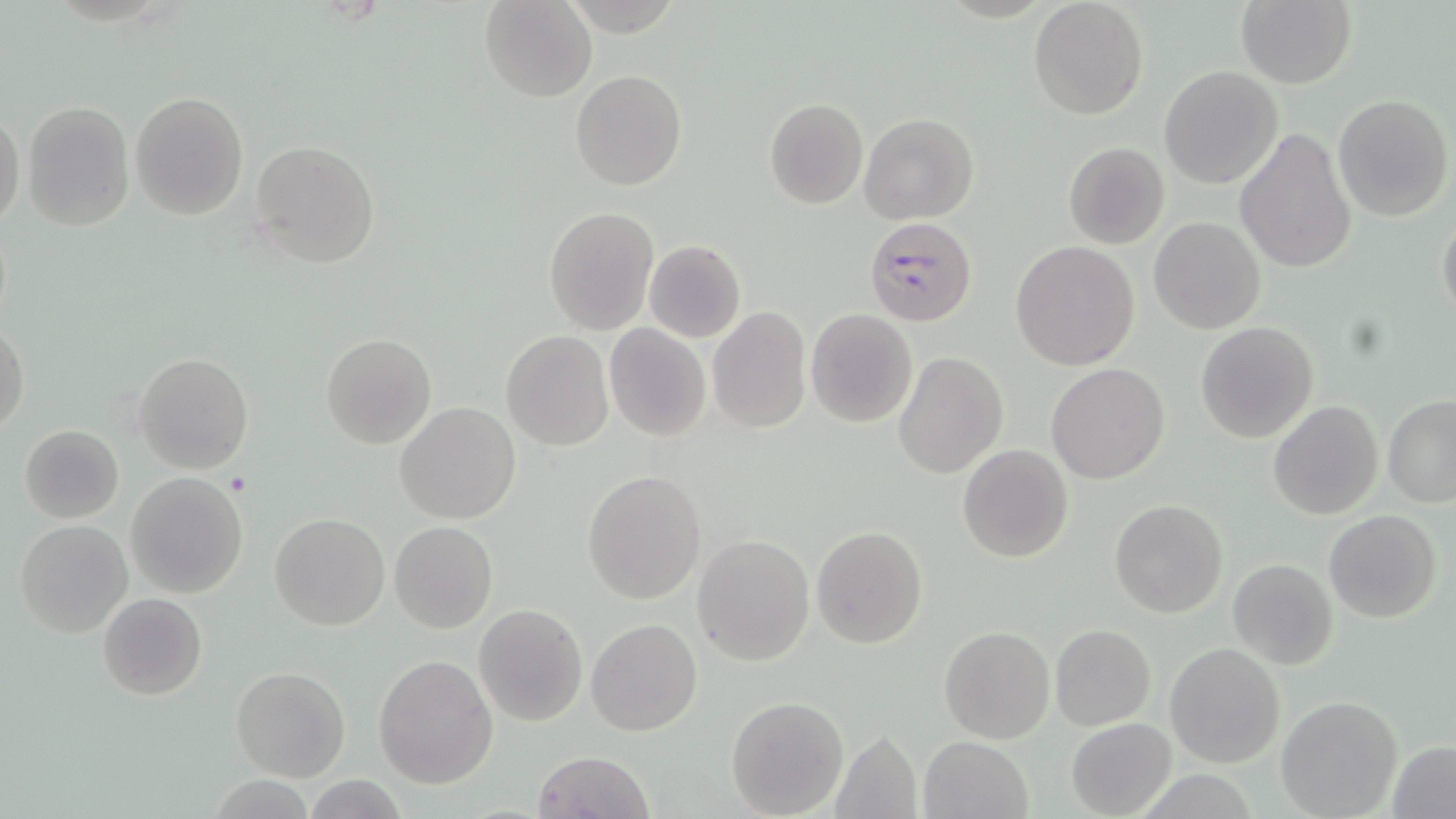

slide-level diagnosis = Plasmodium falciparum
preparation = thin blood smear
magnification = 1000x
image size = 1456×819 pixels
uninfected red blood cell locations (subset) = approximate bounding boxes as (x1, y1, x2, y2) in pixels: (479, 0, 597, 102), (1028, 0, 1149, 119), (1235, 1, 1356, 88), (1159, 66, 1284, 188), (570, 69, 687, 190), (130, 91, 249, 221), (1333, 94, 1453, 222), (764, 99, 867, 208), (22, 101, 136, 230), (1, 110, 25, 229), (859, 112, 979, 224), (1236, 127, 1356, 273), (250, 139, 379, 268), (1062, 141, 1169, 250), (543, 205, 659, 335), (1437, 211, 1456, 326), (1149, 217, 1264, 335), (644, 240, 746, 343), (1011, 241, 1139, 369), (706, 308, 811, 432), (805, 309, 918, 427), (1195, 321, 1320, 443), (0, 324, 28, 437), (605, 324, 712, 442), (501, 330, 613, 450), (319, 332, 436, 450), (894, 350, 1006, 479), (133, 352, 254, 475), (1047, 363, 1169, 484), (1382, 396, 1456, 508), (1267, 400, 1383, 520), (395, 402, 520, 524), (19, 424, 124, 523), (957, 445, 1073, 564), (583, 470, 707, 605), (125, 472, 249, 598), (1111, 501, 1227, 619), (1325, 511, 1441, 623), (269, 512, 390, 629), (16, 519, 132, 638), (389, 522, 497, 633), (811, 525, 928, 649), (692, 534, 813, 666), (1228, 560, 1337, 670), (98, 593, 206, 700), (474, 604, 587, 726), (586, 618, 703, 736), (1050, 624, 1155, 730), (938, 626, 1054, 744), (1165, 643, 1284, 767), (373, 654, 498, 788), (230, 665, 350, 781), (725, 696, 850, 818), (1276, 696, 1403, 818), (1066, 719, 1175, 817), (830, 729, 925, 819), (919, 736, 1032, 819), (1387, 739, 1456, 818), (532, 750, 653, 819)
stain = May-Grünwald-Giemsa
platelet locations = approximate bounding boxes as (x1, y1, x2, y2) in pixels: (223, 470, 251, 496)
field of view = one of a larger specimen
modality = optical microscopy